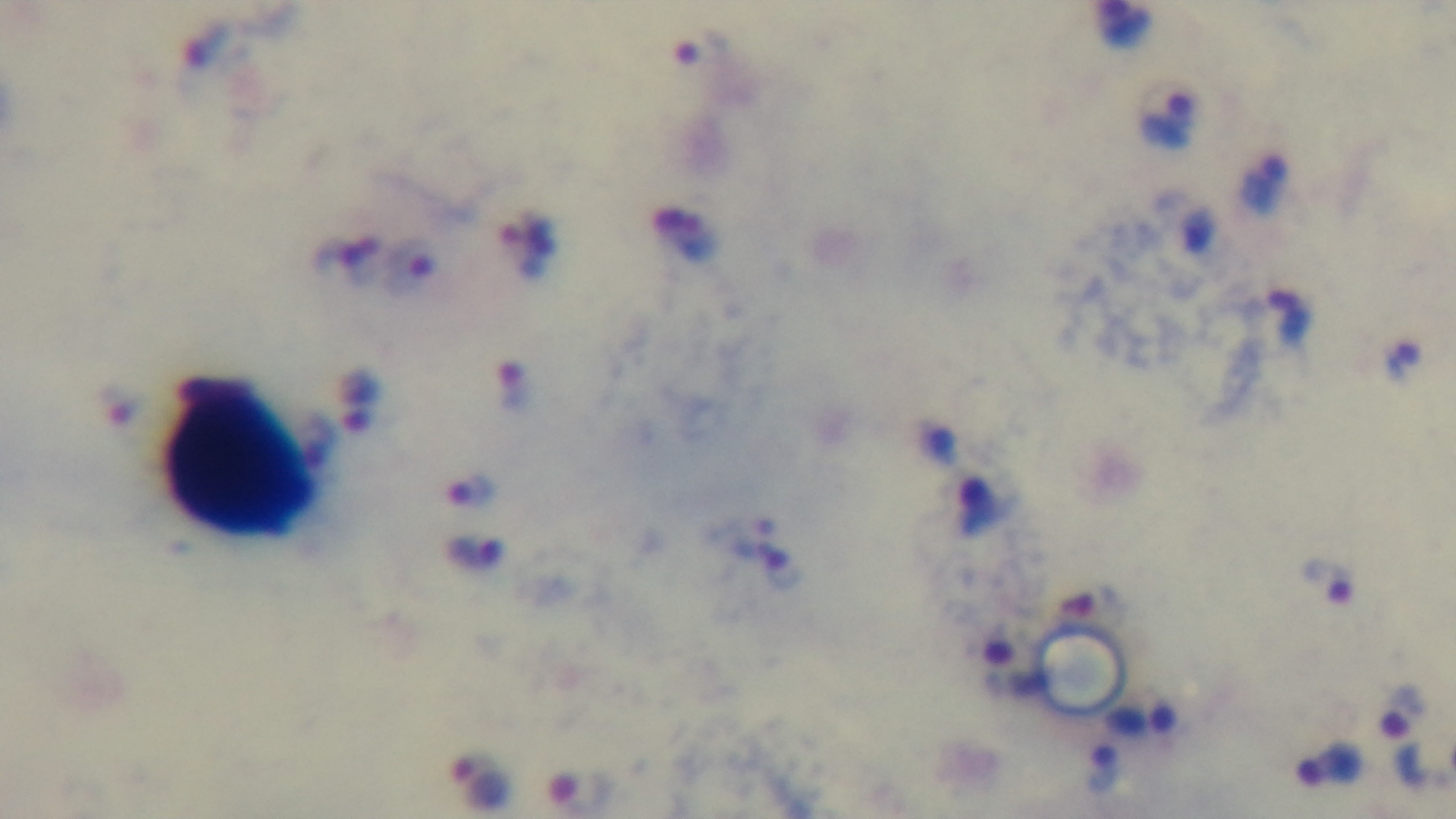
Summary:
  - Modality: light microscopy
  - Objective: 100x oil immersion
  - Field of view: one from the slide
  - Stain: Giemsa
  - Malaria status: positive
  - Capture: mounted 4K digital camera
  - Preparation: thick blood film